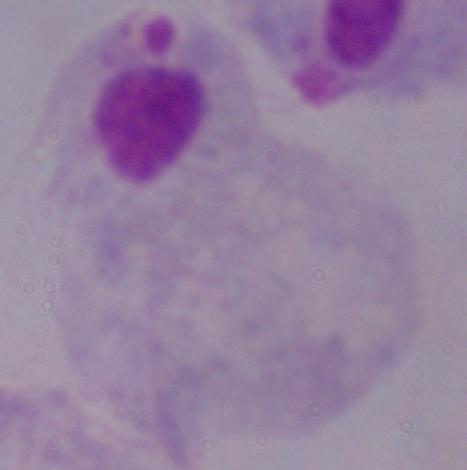
modality = micrograph
magnification = 1000x
identification = trichomonad